Name the parasite shown.
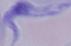
This is a trypanosome.

{
  "modality": "photomicrograph",
  "magnification": "1000x"
}